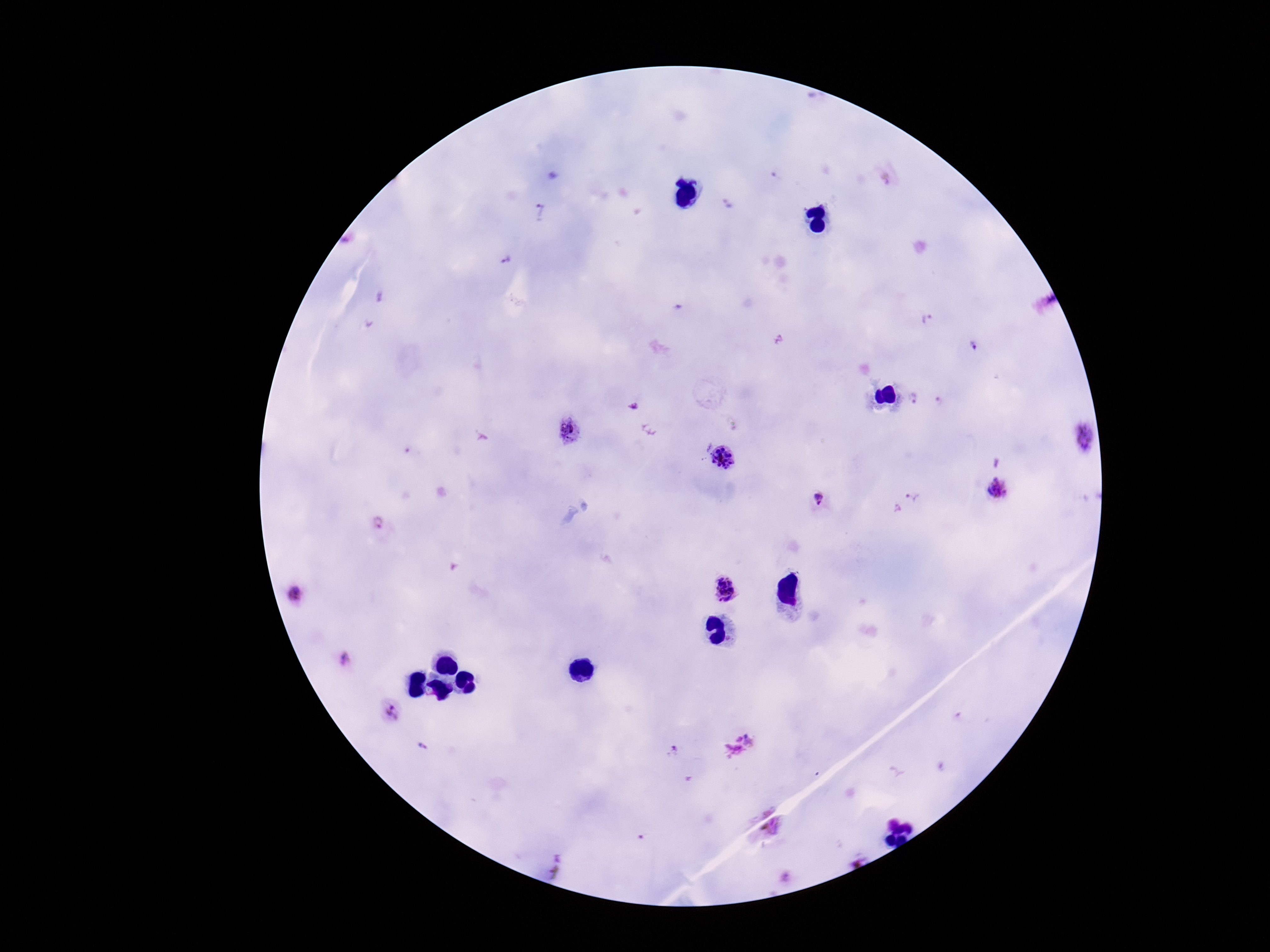

{
  "plasmodium_parasite_locations": "approximate object centers, in pixels from the top-left corner: (x=886, y=174), (x=725, y=204), (x=541, y=212), (x=344, y=241), (x=505, y=261), (x=928, y=320), (x=779, y=339), (x=973, y=348), (x=914, y=399), (x=939, y=403), (x=634, y=406), (x=570, y=430), (x=1084, y=438), (x=722, y=457), (x=995, y=462), (x=998, y=487), (x=915, y=495), (x=818, y=500), (x=382, y=525), (x=726, y=590), (x=296, y=594), (x=345, y=660), (x=390, y=712), (x=741, y=742), (x=423, y=746), (x=672, y=751), (x=770, y=824)",
  "preparation": "thick blood film",
  "patient_malaria_status": "infected",
  "image_size": "1270×952 pixels",
  "field_of_view": "single",
  "stain": "Giemsa",
  "magnification": "100x",
  "capture": "smartphone camera through the microscope eyepiece"
}